Outline each blood parasite and name the species.
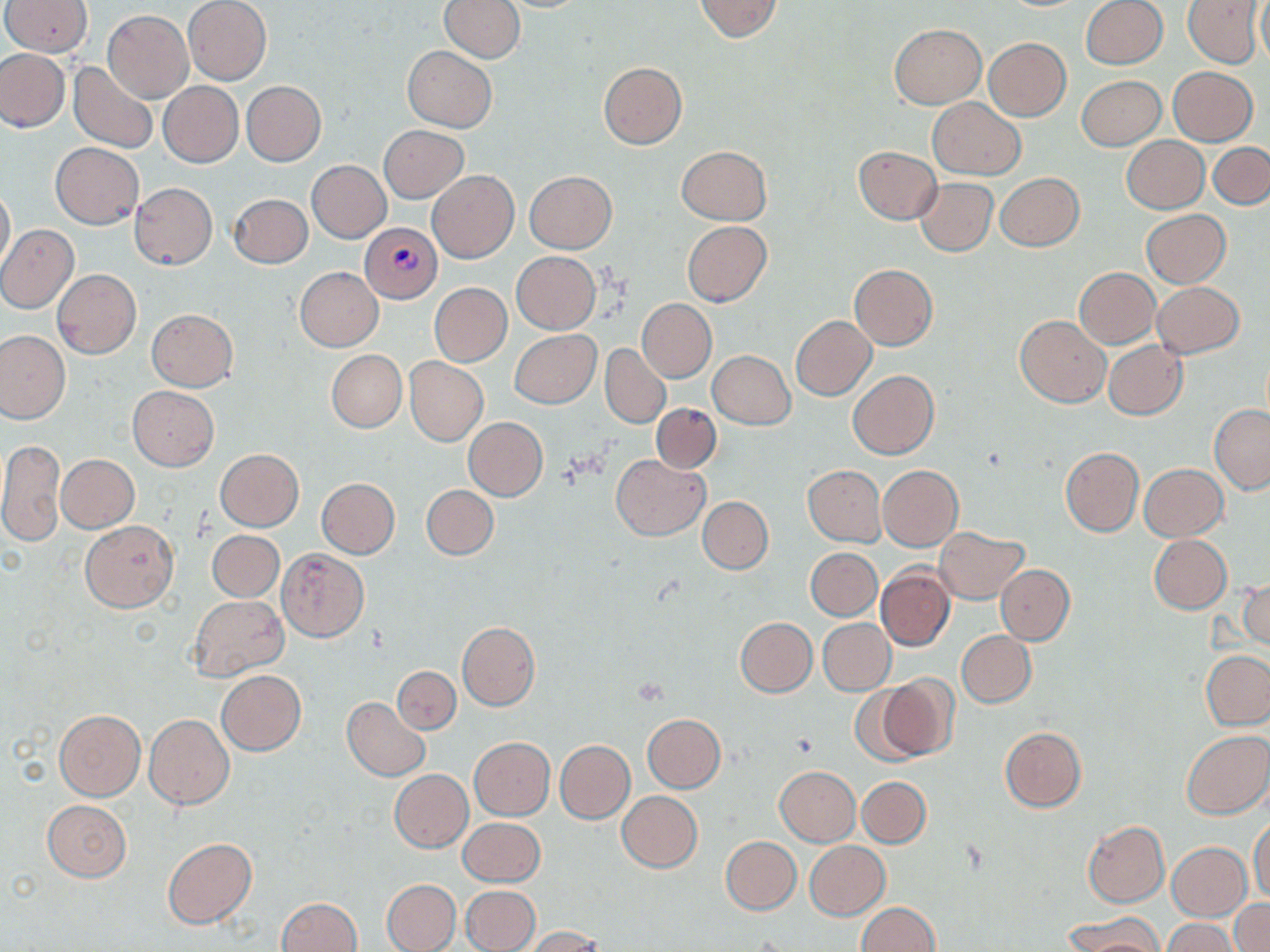
Approximate bounding boxes as [x1, y1, x2, y2] in pixels.
Plasmodium vivax-infected red blood cells: [360, 223, 443, 303].
No Plasmodium falciparum, Plasmodium ovale, Plasmodium malariae, Babesia divergens, or Trypanosoma brucei observed.

Summary:
  - Uninfected red blood cell locations: [439, 0, 524, 62], [693, 0, 783, 43], [1082, 0, 1167, 68], [1179, 0, 1259, 139], [1184, 0, 1263, 67], [1255, 0, 1270, 68], [3, 1, 92, 57], [183, 1, 272, 85], [102, 10, 193, 102], [889, 24, 985, 107], [983, 38, 1071, 121], [402, 46, 496, 131], [0, 49, 69, 131], [598, 61, 687, 150], [68, 62, 159, 154], [1168, 67, 1257, 145], [1076, 75, 1166, 150], [241, 81, 326, 166], [158, 82, 242, 167], [927, 98, 1025, 180], [379, 125, 468, 203], [1122, 136, 1209, 213], [51, 142, 144, 230], [1208, 143, 1270, 209], [677, 146, 771, 225], [853, 147, 941, 223], [307, 161, 391, 242], [427, 170, 519, 264], [524, 171, 618, 253], [996, 172, 1084, 251], [913, 178, 997, 256], [130, 182, 217, 270], [0, 185, 14, 273], [229, 193, 312, 268], [1140, 210, 1230, 288], [682, 221, 771, 307], [0, 224, 79, 314], [511, 251, 600, 333], [850, 264, 937, 349], [295, 267, 383, 351], [1073, 267, 1160, 348], [53, 269, 141, 358], [430, 282, 511, 366], [1152, 282, 1245, 358], [638, 298, 716, 381], [147, 309, 238, 391], [790, 314, 876, 400], [1015, 314, 1111, 408], [510, 329, 601, 408], [0, 331, 69, 423], [1104, 340, 1188, 420], [601, 345, 670, 428], [326, 350, 407, 432], [709, 350, 794, 429], [405, 357, 488, 446], [848, 370, 939, 460], [128, 386, 219, 470], [651, 404, 721, 473], [1209, 405, 1270, 494], [464, 418, 547, 500], [0, 437, 66, 549], [1060, 446, 1144, 536], [215, 449, 304, 531], [611, 454, 709, 540], [57, 455, 138, 532], [878, 464, 964, 552], [1139, 464, 1228, 541], [804, 466, 886, 546], [315, 478, 400, 558], [422, 484, 498, 560], [698, 496, 773, 573], [80, 521, 179, 612], [933, 527, 1030, 603], [207, 531, 284, 602], [1149, 536, 1231, 613], [277, 548, 368, 641], [807, 548, 881, 620], [996, 564, 1075, 643], [877, 566, 955, 651], [1240, 576, 1269, 652], [189, 595, 288, 679], [734, 617, 816, 697], [818, 619, 895, 695], [456, 622, 540, 711], [957, 630, 1036, 707], [1201, 650, 1270, 730], [392, 666, 460, 734], [215, 670, 305, 755], [877, 676, 960, 761], [846, 683, 930, 766], [342, 697, 430, 781], [54, 710, 145, 801], [643, 714, 725, 792], [145, 715, 234, 810], [1000, 726, 1087, 812], [1181, 730, 1270, 819], [470, 737, 555, 820], [555, 740, 635, 823], [774, 766, 861, 845], [389, 769, 473, 851], [857, 777, 931, 847], [616, 790, 703, 873], [41, 799, 132, 881], [458, 818, 546, 887], [1249, 820, 1270, 903], [1082, 821, 1169, 907], [720, 836, 801, 915], [162, 838, 257, 929], [803, 841, 890, 920], [1167, 842, 1252, 921], [381, 879, 460, 951], [461, 884, 540, 952], [277, 897, 362, 952], [1230, 900, 1270, 952], [856, 902, 939, 952], [1185, 909, 1270, 952], [1064, 913, 1163, 952], [1164, 919, 1241, 952], [522, 926, 605, 952]
  - Slide-level diagnosis: Plasmodium vivax
  - Modality: optical microscopy
  - Preparation: thin blood smear
  - Stain: May-Grünwald-Giemsa
  - Image size: 1270×952 pixels
  - Field of view: single
  - Magnification: 1000x